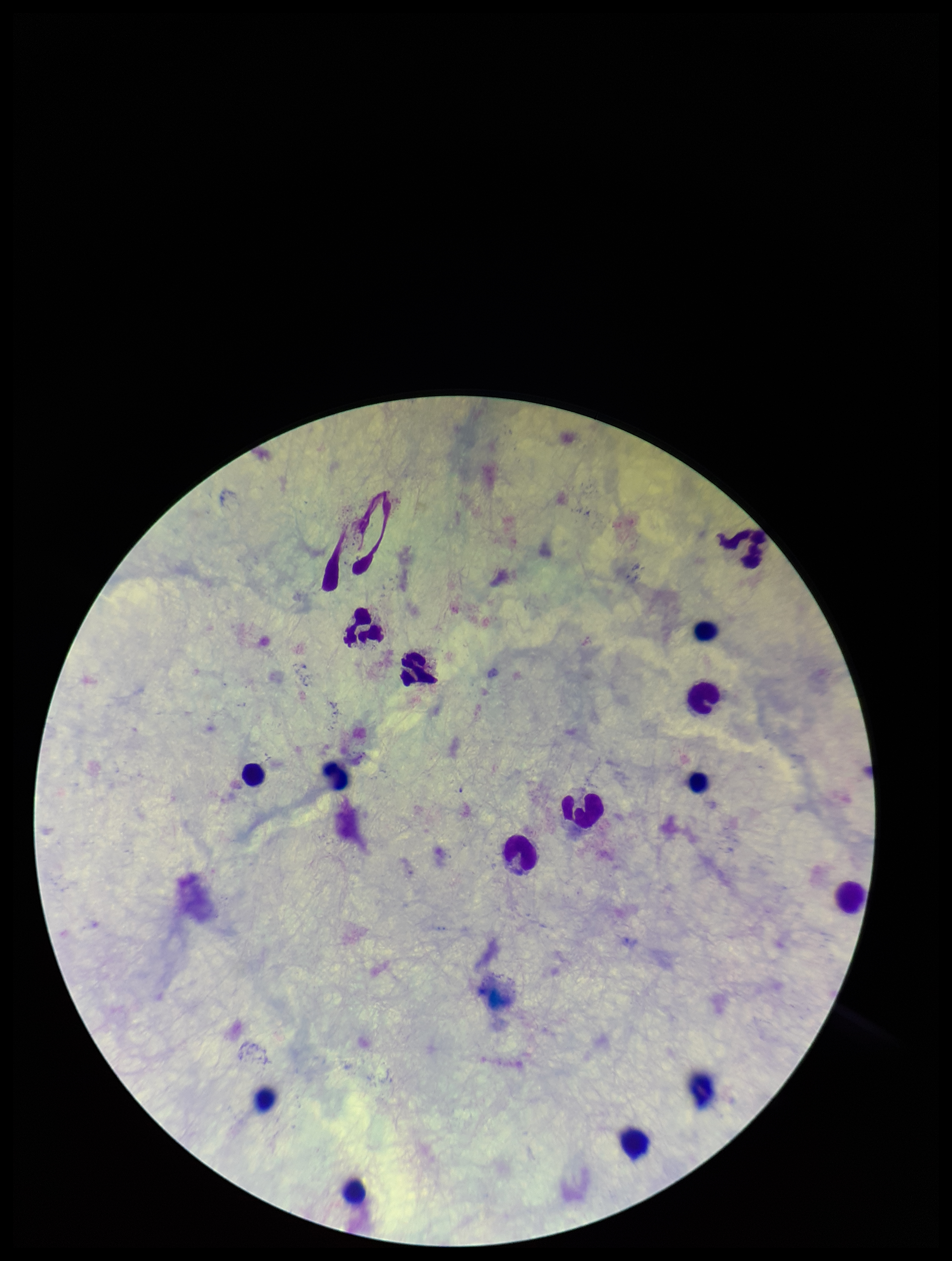
{
  "preparation": "thick",
  "stain": "Giemsa",
  "leukocyte_count": 15,
  "patient_malaria_status": "negative",
  "field_of_view": "single",
  "image_size": "952×1261 pixels",
  "capture": "smartphone photograph through the microscope eyepiece",
  "plasmodium_parasites": "none identified",
  "parasite_count": 0
}